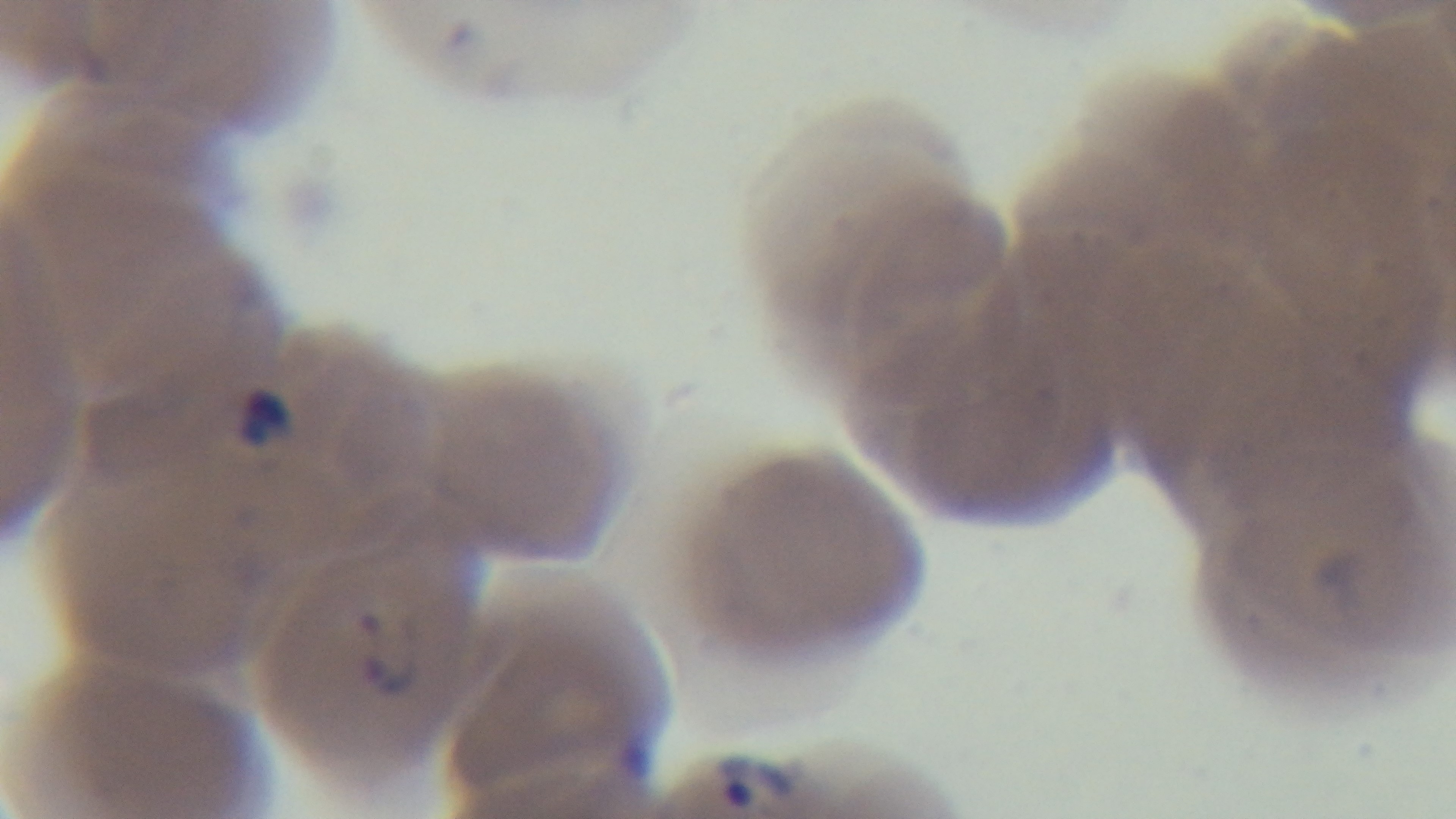

objective = 100x oil immersion
preparation = thin blood film
stain = Giemsa
modality = light microscopy
field of view = one from the slide
malaria status = infected
capture = mounted 4K digital camera